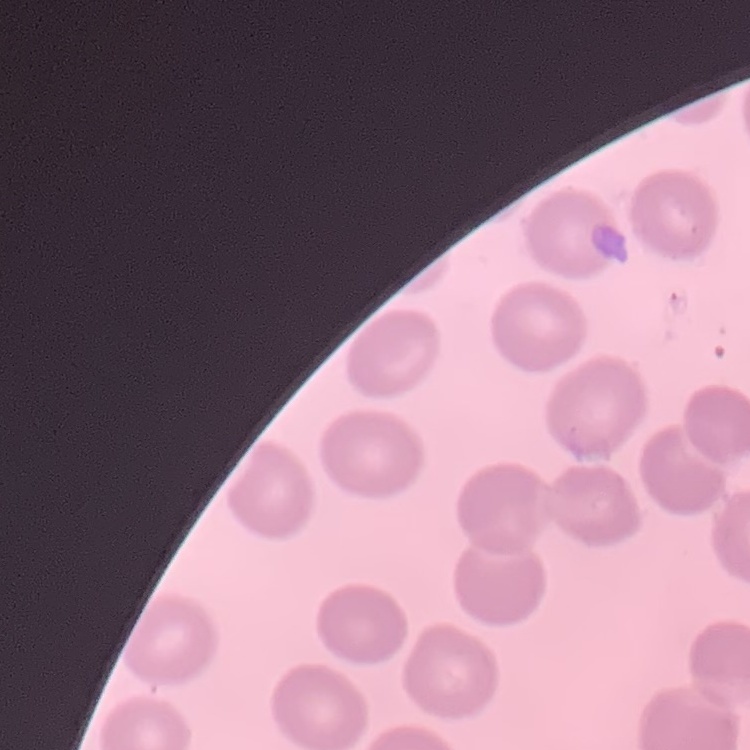 The red blood cells show no rouleaux formation. Thin peripheral smear. Square crop of a larger photomicrograph. Field's or Giemsa stain.